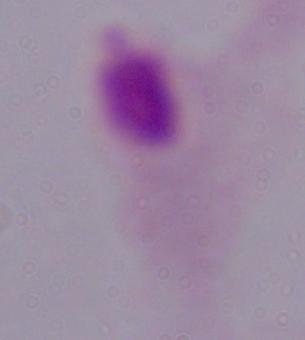
magnification = 1000x
modality = micrograph
identification = trichomonad